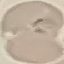
Summary:
  - Result: malaria parasites identified
  - Image type: cell patch, automatically extracted from a larger field of view and resized to 64 × 64 pixels
  - Preparation: thin blood film
  - Capture: smartphone through the microscope eyepiece
  - Stain: Giemsa